Classify this cell by malaria status.
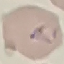
It is parasitized.

Photographed with a smartphone camera at the microscope eyepiece. Thin blood smear. Giemsa-stained preparation. Automatically extracted cell patch, resized to 64 × 64 pixels.